Describe the morphology of the red blood cells.
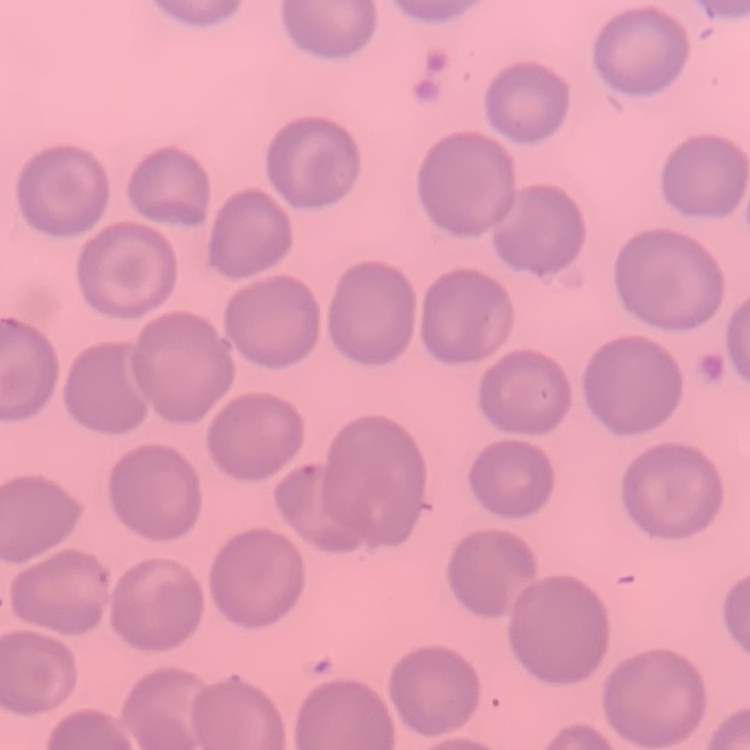

No rouleaux formation.

Summary:
  - Image type: one tile cut from a larger photomicrograph
  - Preparation: thin peripheral smear
  - Stain: Field's or Giemsa